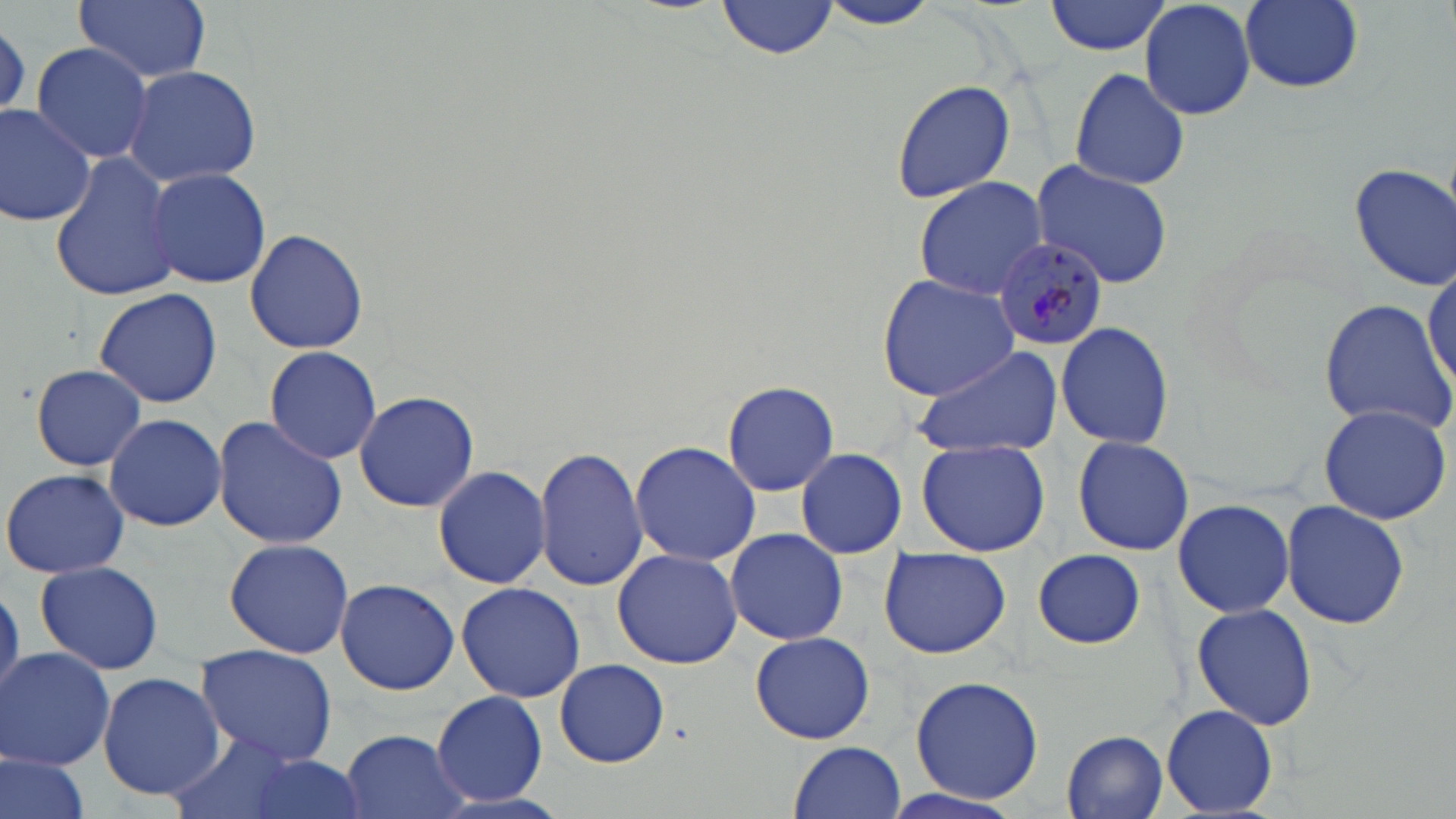

plasmodium_malariae_infected_red_blood_cell_locations: 'approximate bounding boxes as named x1/y1/x2/y2 corners in pixels: (x1=992, y1=237, x2=1108, y2=351)'
slide_level_diagnosis: Plasmodium malariae
modality: light microscopy
field_of_view: single
stain: May-Grünwald-Giemsa
magnification: 1000x
preparation: thin blood smear
uninfected_red_blood_cell_locations: 'approximate bounding boxes as named x1/y1/x2/y2 corners in pixels: (x1=74, y1=0, x2=211, y2=83), (x1=718, y1=0, x2=839, y2=58), (x1=1045, y1=0, x2=1172, y2=56), (x1=1139, y1=0, x2=1257, y2=120), (x1=1240, y1=0, x2=1364, y2=92), (x1=815, y1=1, x2=948, y2=31), (x1=31, y1=42, x2=155, y2=164), (x1=123, y1=64, x2=263, y2=188), (x1=1066, y1=65, x2=1192, y2=192), (x1=889, y1=79, x2=1017, y2=204), (x1=0, y1=104, x2=98, y2=227), (x1=50, y1=154, x2=184, y2=302), (x1=1029, y1=157, x2=1175, y2=290), (x1=1348, y1=163, x2=1456, y2=288), (x1=146, y1=166, x2=271, y2=288), (x1=913, y1=177, x2=1051, y2=299), (x1=245, y1=229, x2=368, y2=355), (x1=1424, y1=259, x2=1456, y2=397), (x1=876, y1=276, x2=1023, y2=401), (x1=92, y1=287, x2=223, y2=408), (x1=1318, y1=298, x2=1455, y2=434), (x1=1055, y1=319, x2=1175, y2=452), (x1=914, y1=342, x2=1063, y2=459), (x1=263, y1=346, x2=382, y2=464), (x1=30, y1=363, x2=147, y2=471), (x1=722, y1=379, x2=840, y2=496), (x1=353, y1=390, x2=479, y2=513), (x1=1317, y1=402, x2=1453, y2=525), (x1=104, y1=412, x2=227, y2=532), (x1=213, y1=416, x2=347, y2=550), (x1=1072, y1=435, x2=1195, y2=555), (x1=917, y1=438, x2=1052, y2=557), (x1=630, y1=441, x2=763, y2=567), (x1=532, y1=446, x2=649, y2=592), (x1=795, y1=448, x2=907, y2=559), (x1=434, y1=462, x2=552, y2=590), (x1=2, y1=467, x2=131, y2=579), (x1=1172, y1=497, x2=1295, y2=620), (x1=1280, y1=499, x2=1410, y2=631), (x1=726, y1=529, x2=849, y2=644), (x1=224, y1=538, x2=354, y2=658), (x1=877, y1=547, x2=1014, y2=660), (x1=613, y1=548, x2=742, y2=669), (x1=1031, y1=549, x2=1146, y2=649), (x1=34, y1=559, x2=164, y2=675), (x1=333, y1=580, x2=460, y2=695), (x1=457, y1=581, x2=586, y2=702), (x1=0, y1=586, x2=22, y2=703), (x1=1192, y1=603, x2=1318, y2=730), (x1=750, y1=631, x2=875, y2=744), (x1=193, y1=644, x2=339, y2=765), (x1=1, y1=647, x2=116, y2=771), (x1=553, y1=659, x2=669, y2=766), (x1=97, y1=672, x2=224, y2=798), (x1=909, y1=675, x2=1045, y2=805), (x1=431, y1=690, x2=547, y2=805), (x1=1162, y1=705, x2=1279, y2=815), (x1=166, y1=729, x2=301, y2=819), (x1=336, y1=729, x2=471, y2=819), (x1=1063, y1=731, x2=1169, y2=816), (x1=789, y1=742, x2=907, y2=819), (x1=1, y1=750, x2=93, y2=819), (x1=231, y1=755, x2=373, y2=819), (x1=874, y1=785, x2=1026, y2=819)'
image_size: 1456×819 pixels